Assess this cell for malaria.
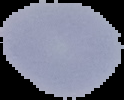

Parasitized.

image size = 124×100 pixels
image type = segmented cell region with the area outside set to black
preparation = thin blood film